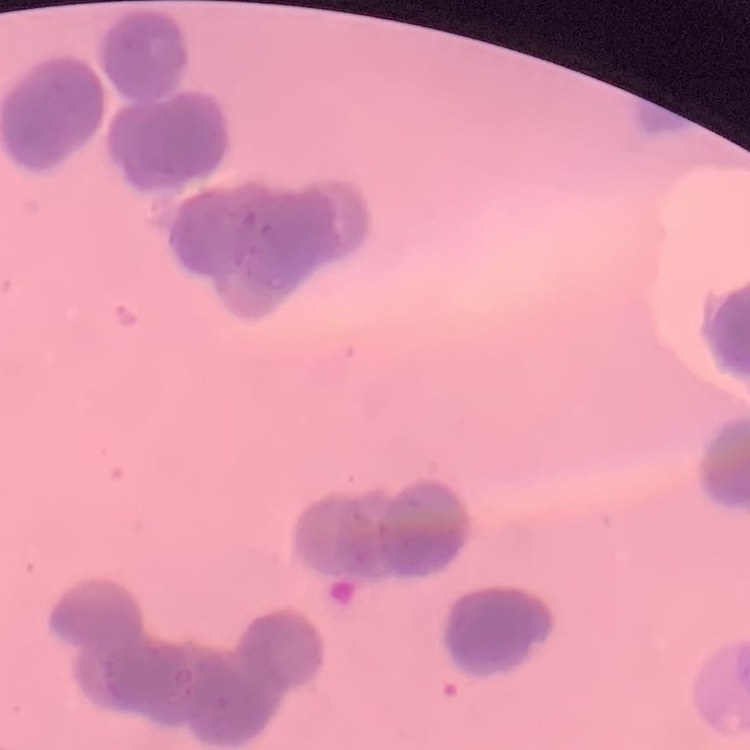

Summary:
  - Red blood cell morphology: rouleaux formation
  - Image type: square crop of a larger photomicrograph
  - Preparation: thin peripheral smear
  - Stain: Field's or Giemsa